Comment on the morphology of the erythrocytes.
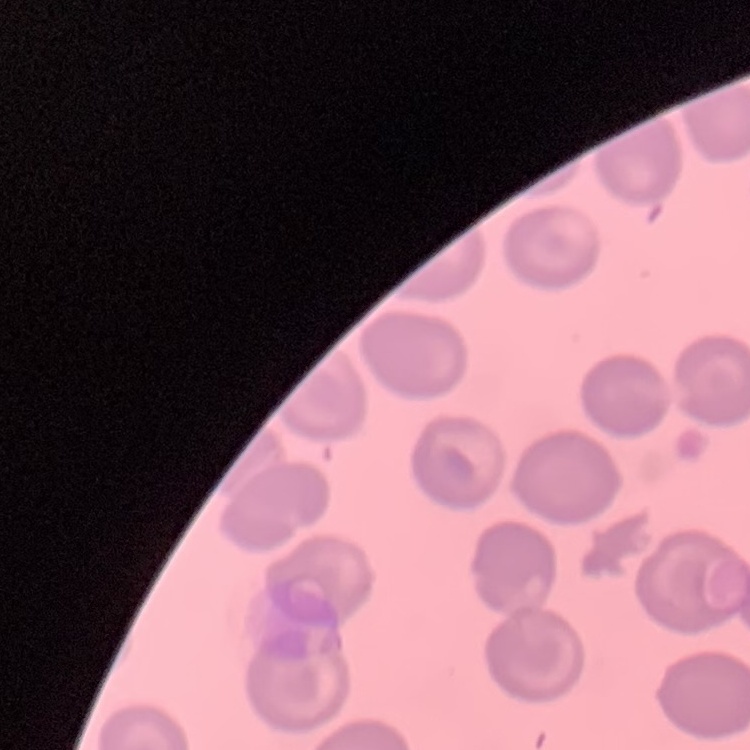
They show no rouleaux formation.

preparation: thin peripheral smear
image_type: one tile cut from a larger photomicrograph
stain: Field's or Giemsa